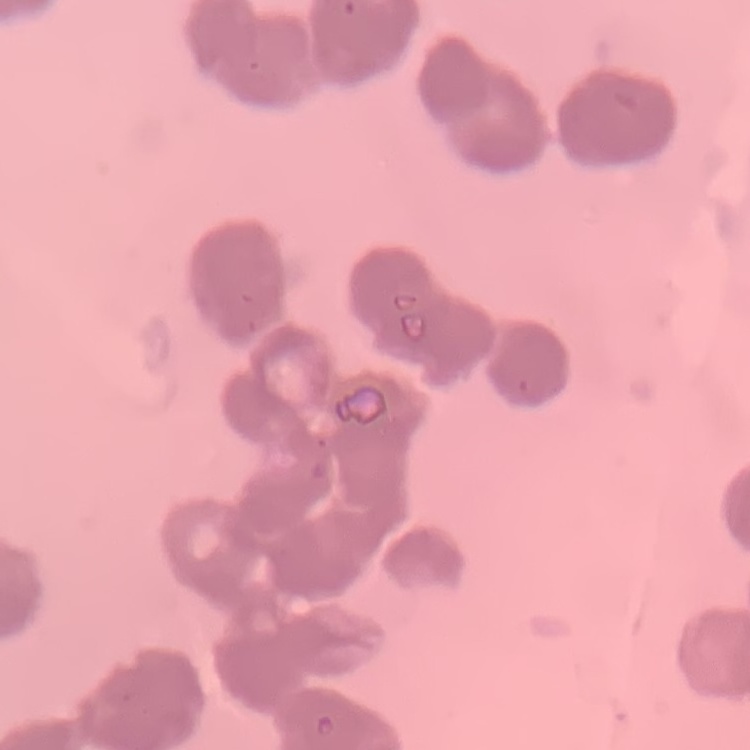

The red blood cells show rouleaux formation. Stained with either Field's or Giemsa. Thin peripheral smear. One tile cut from a larger photomicrograph.